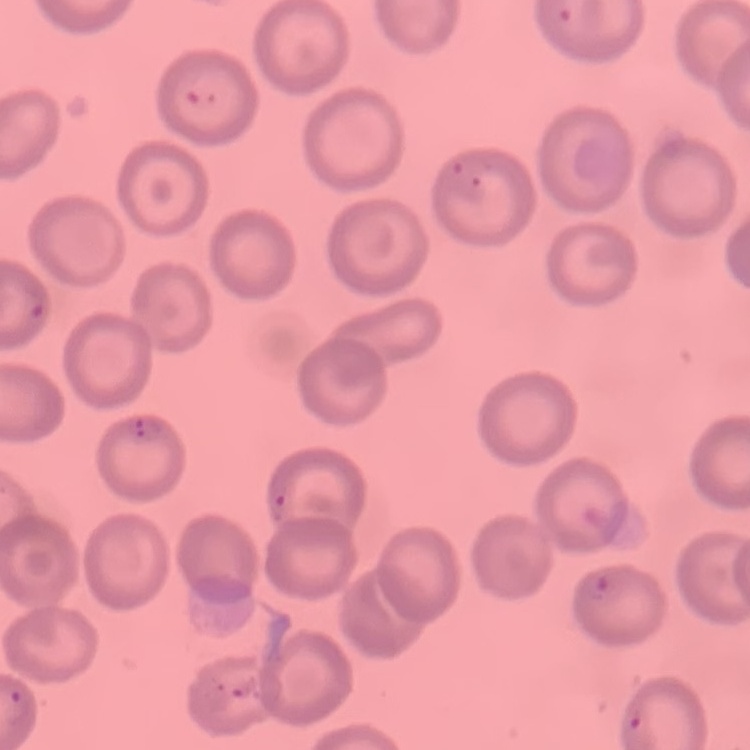 The erythrocytes exhibit no rouleaux formation. Thin blood smear. One tile cut from a larger photomicrograph. Field's or Giemsa stain.